Classify this cell by malaria status.
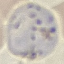

It is parasitized.

Thin smear of blood. Giemsa-stained preparation. Photographed with a smartphone camera at the microscope eyepiece. Cell patch, automatically extracted from a larger field of view and resized to 64 × 64 pixels.